Locate every Plasmodium parasite.
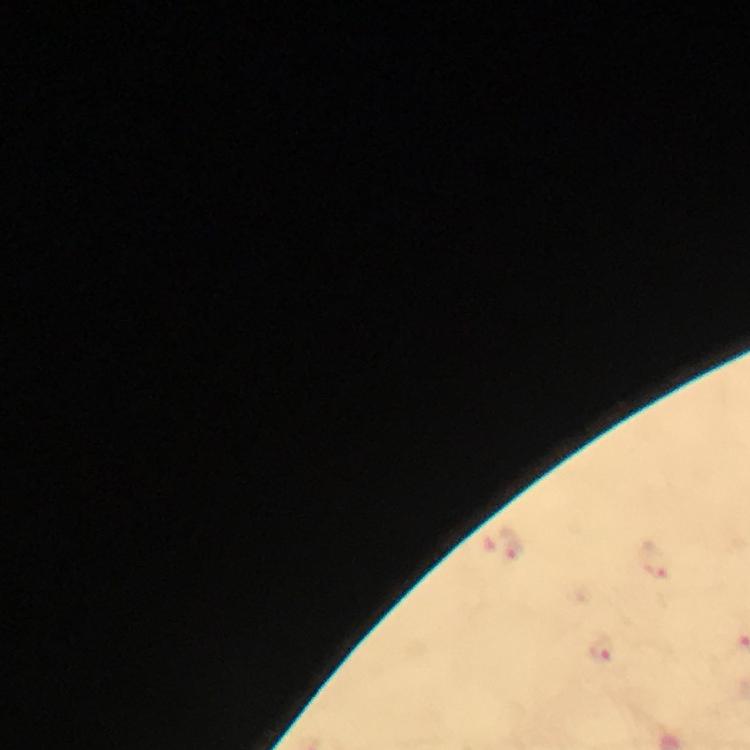

Approximate centers as {x, y} in pixels.
Plasmodium parasites: {511, 547}, {655, 562}, {599, 650}.

{
  "immersion_oil": "used",
  "image_size": "750×750 pixels",
  "magnification": "100x",
  "preparation": "thick smear",
  "context": "from a malaria diagnostic workup",
  "cropped_from": "one field of view",
  "capture": "smartphone photograph through a microscope",
  "stain": "Giemsa"
}